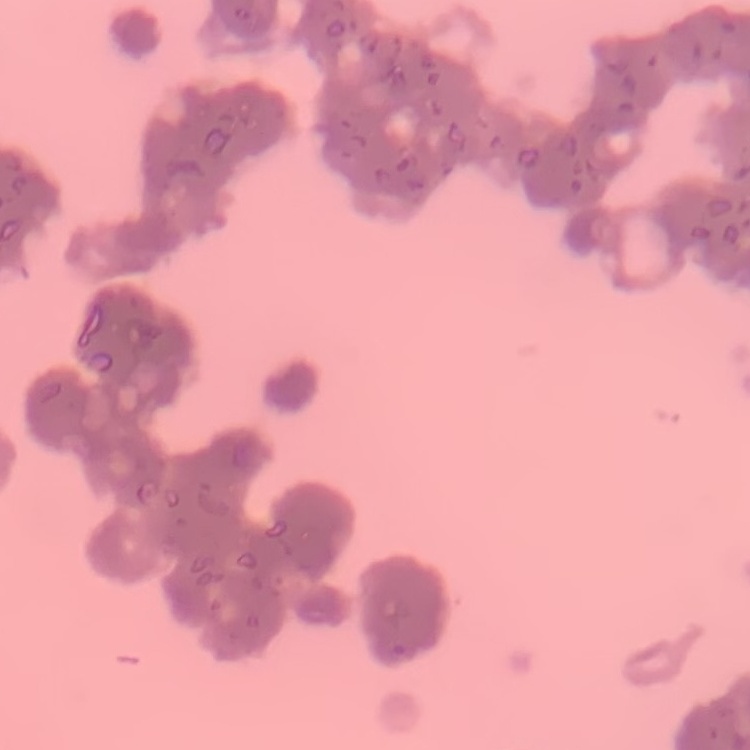

red blood cell morphology = rouleaux formation
preparation = thin peripheral smear
image type = one tile cut from a larger photomicrograph
stain = Field's or Giemsa